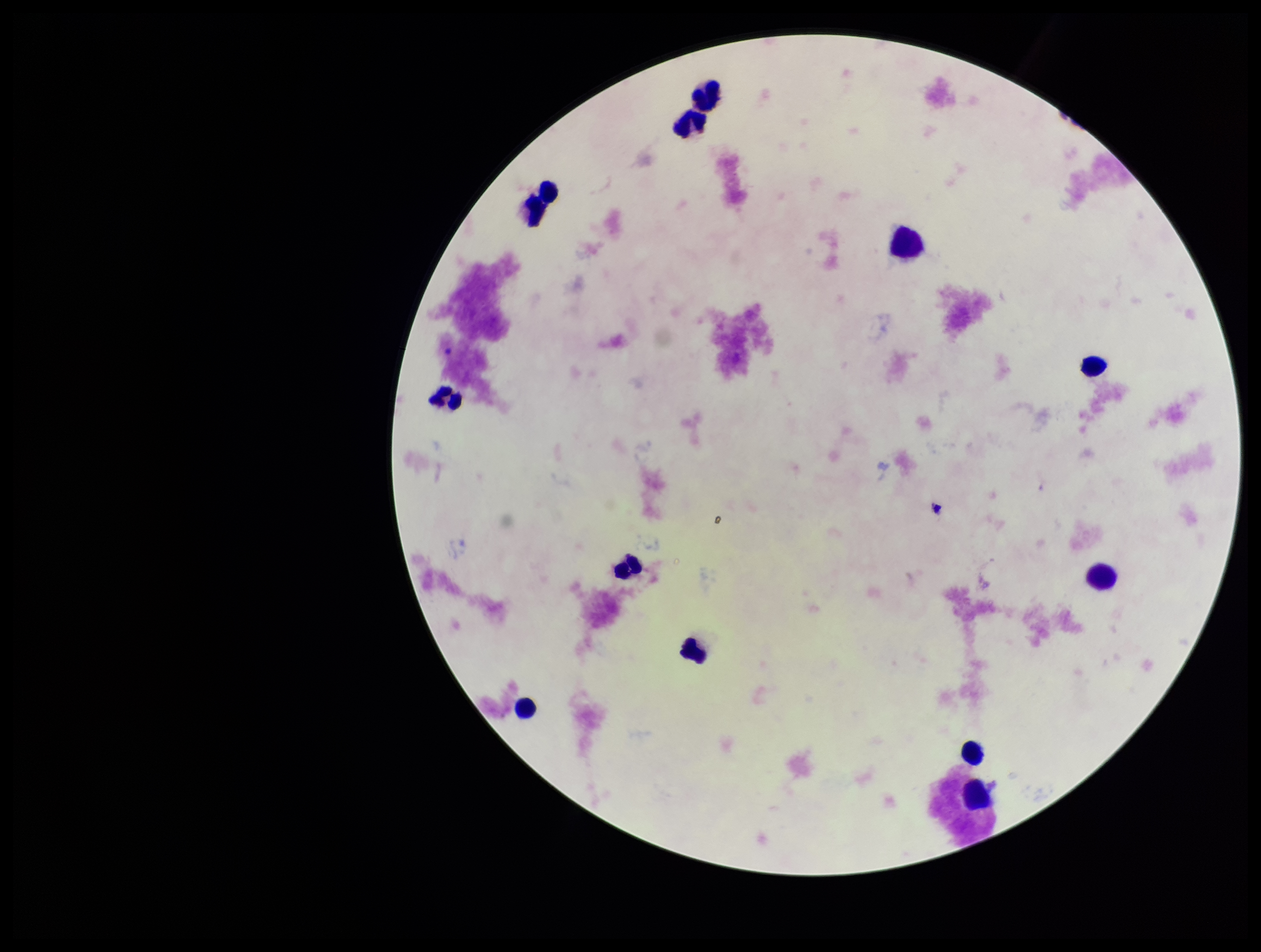
Preparation: thick blood smear. Single field of view. Leukocyte count: 13. Smartphone photograph taken through the eyepiece of a microscope. Plasmodium parasites: none detected. Image is 1261×952 pixels. Giemsa stain. Parasite count: 0. Patient malaria status: negative.